State the preparation type.
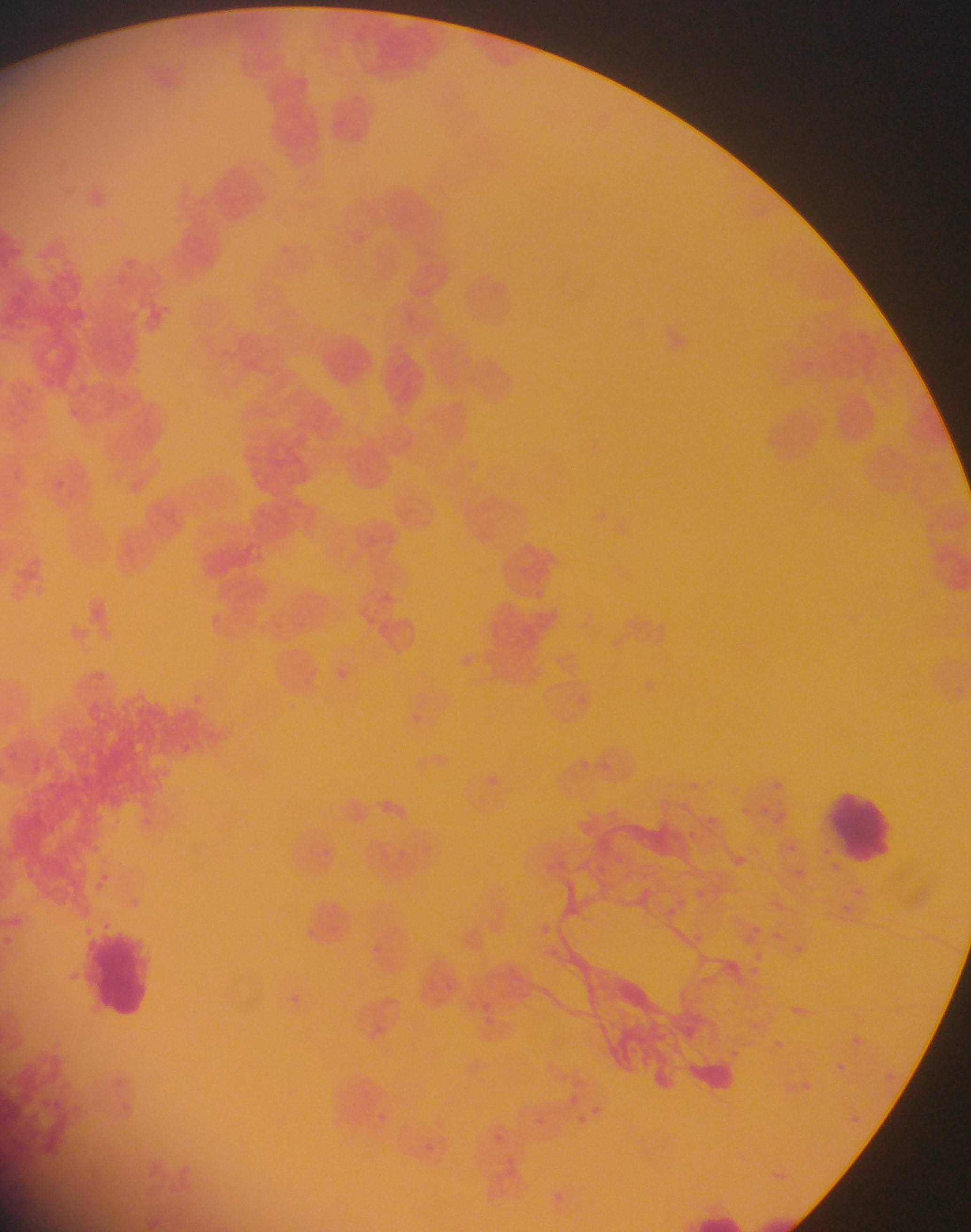

This is a thin smear.

field of view = single
country = Ghana
capture = mobile-phone photograph through a microscope
leukocyte locations = approximate bounding boxes as (left, top, right, bottom) in pixels: (826, 788, 895, 864), (89, 928, 153, 1018)
image size = 971×1232 pixels
Plasmodium parasite locations = approximate bounding boxes as (left, top, right, bottom) in pixels: (274, 240, 294, 258), (575, 751, 602, 776), (772, 774, 786, 795), (699, 811, 722, 834), (766, 815, 790, 828), (794, 864, 805, 879), (695, 885, 705, 894), (840, 899, 853, 922), (752, 918, 762, 935), (795, 940, 804, 954), (754, 944, 768, 957), (725, 954, 746, 976), (848, 1034, 860, 1049), (828, 1058, 848, 1077), (884, 1064, 903, 1083), (796, 1077, 815, 1095), (568, 1090, 587, 1110), (571, 1110, 596, 1130), (536, 1113, 562, 1140)